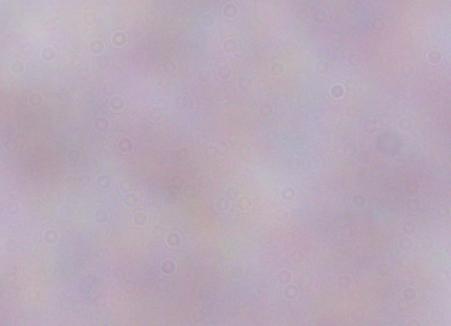
magnification = 1000x
identification = trypanosome
modality = photomicrograph